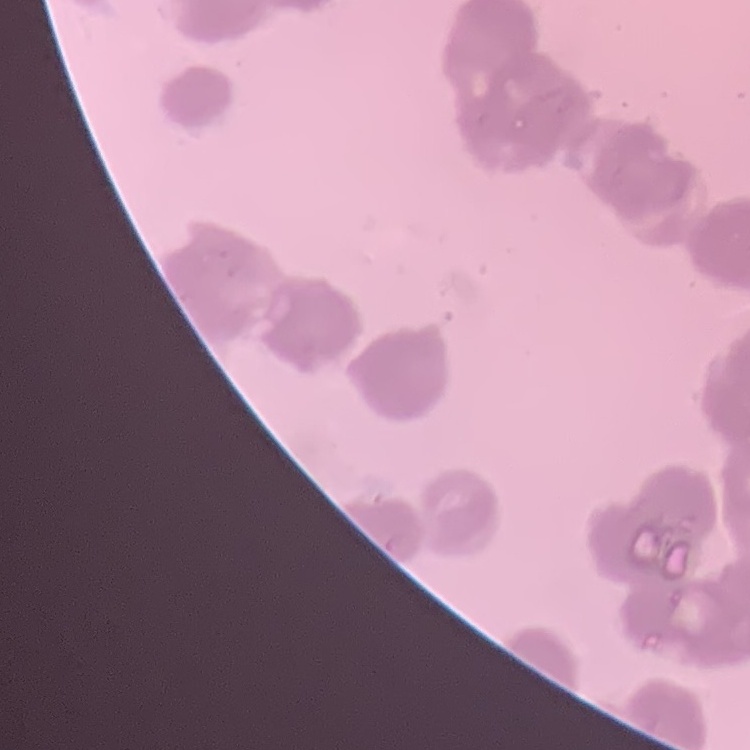
erythrocyte_morphology: rouleaux formation
image_type: square crop of a larger photomicrograph
stain: Field's or Giemsa
preparation: thin blood smear